Locate every Plasmodium falciparum-infected red blood cell.
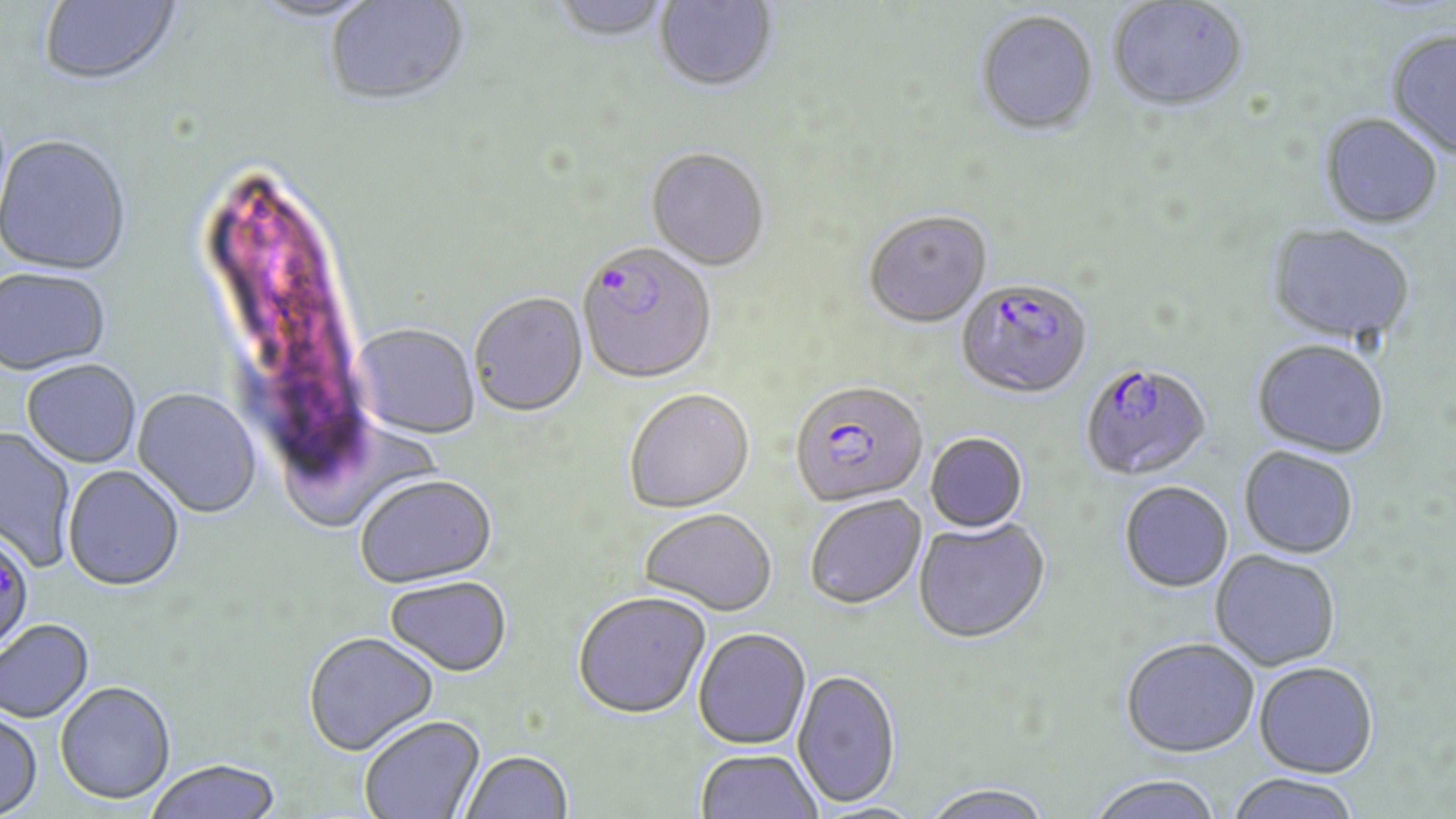

Approximate bounding boxes as [x1, y1, x2, y2] in pixels.
Plasmodium falciparum-infected red blood cells: [577, 244, 717, 387], [956, 280, 1093, 402], [1079, 362, 1213, 483], [790, 383, 928, 510], [0, 530, 34, 656].

slide-level diagnosis = Plasmodium falciparum
preparation = thin blood film
field of view = single
stain = May-Grünwald-Giemsa
image size = 1456×819 pixels
uninfected red blood cell locations = approximate bounding boxes as [x1, y1, x2, y2] in pixels: [38, 0, 181, 89], [248, 0, 383, 26], [324, 0, 471, 110], [550, 0, 673, 44], [654, 0, 778, 94], [1107, 1, 1248, 114], [975, 13, 1099, 138], [1385, 30, 1456, 163], [1319, 116, 1443, 230], [0, 135, 132, 277], [646, 149, 770, 273], [863, 213, 992, 330], [1266, 224, 1416, 348], [0, 268, 112, 376], [469, 293, 588, 419], [350, 324, 481, 441], [1252, 342, 1389, 460], [21, 360, 141, 469], [132, 388, 261, 518], [624, 391, 755, 515], [0, 426, 76, 571], [925, 434, 1029, 534], [1239, 448, 1359, 560], [62, 466, 185, 592], [354, 477, 498, 590], [1119, 483, 1234, 594], [805, 496, 927, 611], [639, 510, 777, 618], [913, 519, 1051, 646], [1210, 551, 1340, 672], [385, 577, 512, 678], [572, 593, 712, 721], [0, 619, 95, 724], [693, 629, 811, 751], [303, 632, 439, 757], [1120, 639, 1259, 760], [1253, 662, 1378, 779], [792, 671, 901, 810], [55, 681, 176, 804], [0, 709, 43, 818], [360, 716, 487, 818], [695, 750, 822, 819], [460, 751, 574, 819], [145, 759, 283, 819], [1224, 774, 1363, 819], [1087, 776, 1224, 819], [918, 785, 1054, 819]
magnification = 1000x
modality = optical microscopy